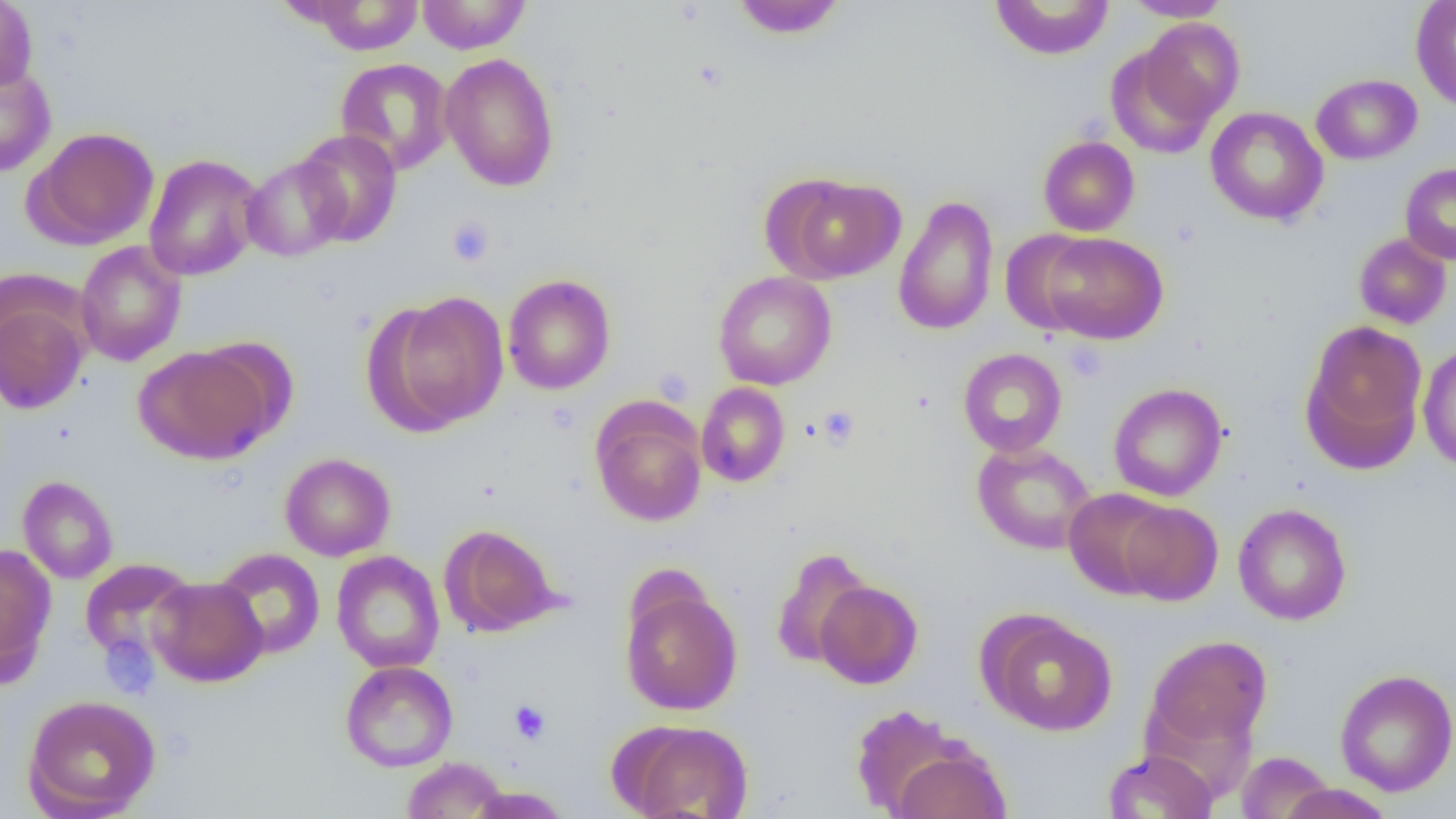

Summary:
  - Coordinate format: approximate bounding boxes as (x1,y1)-(x2,y2) corner pairs in pixels
  - Uninfected red blood cell locations: (0,0)-(37,94), (416,0)-(531,54), (731,0)-(846,38), (989,0)-(1114,61), (1122,0)-(1231,21), (1410,0)-(1456,113), (300,1)-(425,55), (1137,19)-(1244,127), (1105,42)-(1222,158), (440,52)-(559,191), (335,58)-(454,174), (0,61)-(56,177), (1311,74)-(1422,165), (1205,106)-(1328,226), (27,127)-(160,249), (293,129)-(403,246), (1038,136)-(1139,236), (144,154)-(264,281), (241,156)-(349,261), (1399,163)-(1456,265), (769,174)-(906,283), (892,195)-(999,336), (1000,230)-(1098,334), (1037,231)-(1169,344), (1353,233)-(1452,330), (74,241)-(187,367), (713,270)-(837,390), (502,274)-(616,395), (377,291)-(509,432), (1,299)-(89,415), (1300,321)-(1428,473), (1417,342)-(1456,472), (133,344)-(277,464), (958,348)-(1067,457), (696,382)-(790,487), (1108,383)-(1228,502), (591,402)-(707,526), (972,441)-(1097,554), (279,453)-(396,561), (18,476)-(118,584), (1064,488)-(1175,599), (1118,501)-(1223,606), (1232,503)-(1352,625), (440,524)-(562,637), (0,543)-(56,682), (769,547)-(874,670), (212,548)-(326,659), (332,551)-(445,673), (79,558)-(196,665), (147,576)-(267,687), (815,580)-(923,688), (620,584)-(743,715), (982,613)-(1118,736), (1144,635)-(1272,752), (340,660)-(458,772), (1335,668)-(1456,797), (23,694)-(161,818), (849,703)-(973,817), (615,719)-(754,819), (890,742)-(1012,819), (1103,749)-(1219,818), (1235,751)-(1336,818), (401,756)-(509,818), (1275,783)-(1395,819), (466,785)-(572,819)
  - Platelet locations: (446,216)-(495,267), (1063,341)-(1107,382), (653,366)-(695,406), (817,404)-(860,449), (509,700)-(552,743)
  - Slide-level diagnosis: no evidence of blood parasites
  - Magnification: 1000x
  - Modality: optical microscopy
  - Preparation: thin blood smear
  - Image size: 1456×819 pixels
  - Field of view: one of a larger specimen